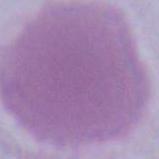

An erythrocyte is seen. Captured at 1000x magnification. Micrograph.